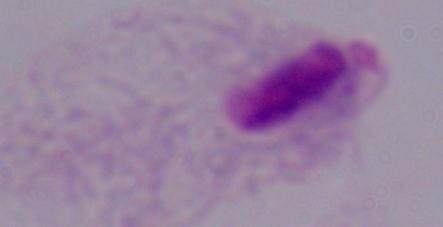
Summary:
  - Identification: trichomonad
  - Magnification: 1000x
  - Modality: photomicrograph